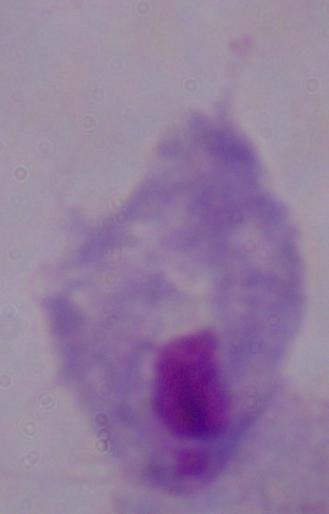

Summary:
  - Magnification: 1000x
  - Modality: photomicrograph
  - Identification: trichomonad